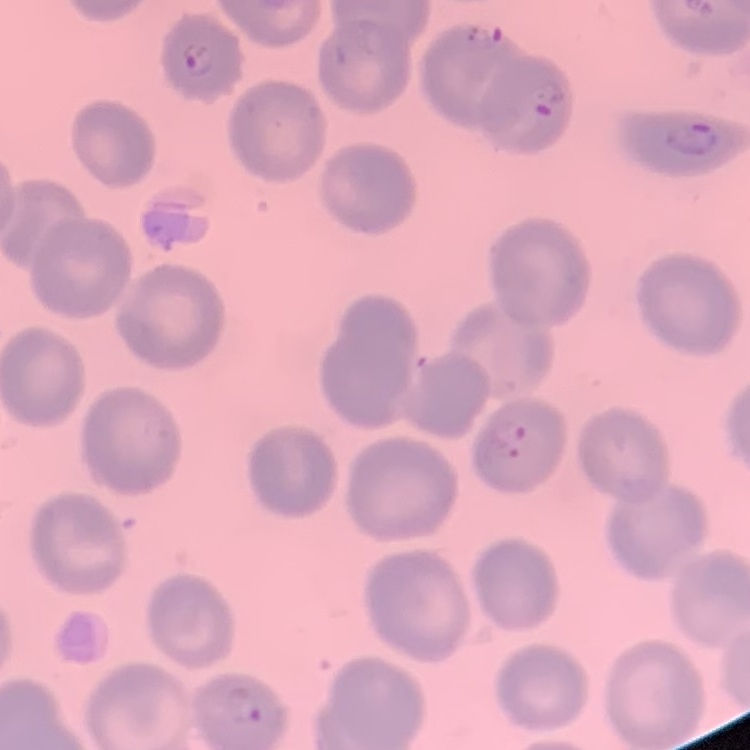

The red blood cells exhibit no rouleaux formation. Square crop of a larger photomicrograph. Thin peripheral smear. Field's or Giemsa stain.